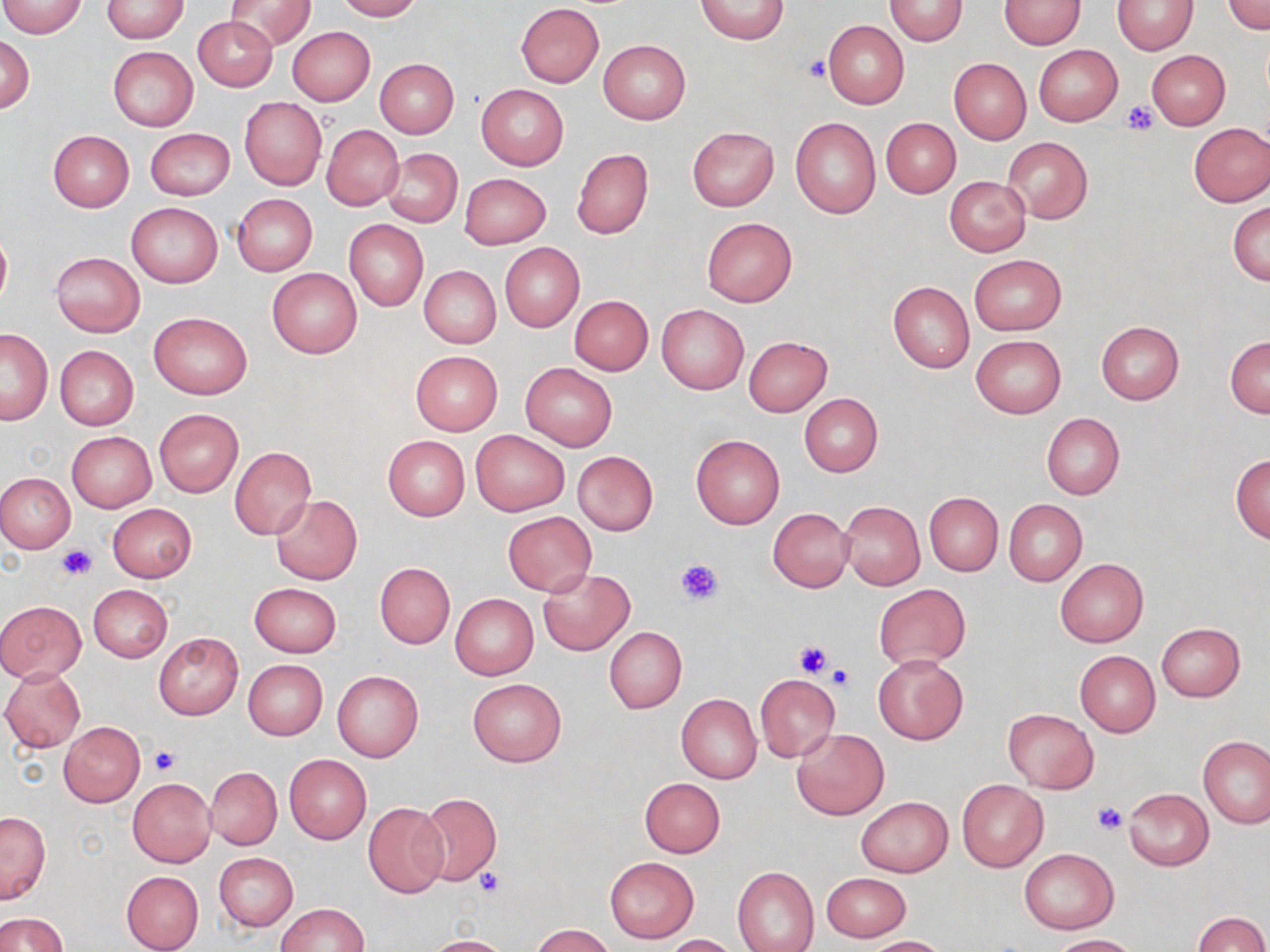
slide-level diagnosis = negative for blood parasites
preparation = thin blood smear
stain = May-Grünwald-Giemsa
image size = 1270×952 pixels
magnification = 1000x
uninfected red blood cell locations = approximate bounding boxes as [x1, y1, x2, y2] in pixels: [226, 0, 315, 51], [333, 0, 421, 21], [694, 0, 791, 45], [883, 0, 968, 45], [1224, 0, 1270, 34], [0, 1, 89, 37], [102, 1, 190, 42], [998, 1, 1086, 49], [1112, 1, 1197, 55], [516, 4, 605, 87], [193, 17, 279, 90], [822, 20, 909, 109], [288, 26, 375, 105], [1, 35, 34, 112], [598, 40, 691, 125], [1033, 44, 1123, 126], [107, 46, 199, 131], [1146, 50, 1230, 130], [949, 57, 1031, 144], [374, 58, 458, 139], [476, 84, 569, 169], [240, 98, 326, 190], [789, 116, 881, 219], [880, 117, 960, 198], [1188, 122, 1270, 206], [321, 124, 404, 210], [687, 126, 779, 211], [146, 127, 234, 200], [48, 130, 133, 212], [1001, 137, 1092, 224], [382, 148, 462, 227], [571, 148, 653, 239], [460, 173, 551, 249], [945, 176, 1032, 257], [232, 194, 317, 276], [1228, 201, 1270, 286], [127, 202, 223, 288], [702, 217, 796, 307], [344, 219, 428, 311], [0, 228, 11, 311], [499, 243, 585, 333], [51, 251, 145, 337], [969, 254, 1066, 335], [419, 266, 501, 349], [267, 268, 362, 358], [888, 281, 974, 373], [569, 295, 653, 376], [657, 305, 749, 393], [148, 311, 252, 398], [1097, 321, 1183, 404], [0, 328, 53, 425], [971, 335, 1066, 418], [742, 336, 833, 416], [1226, 336, 1270, 417], [55, 345, 139, 431], [410, 351, 503, 435], [520, 363, 617, 452], [799, 394, 883, 477], [153, 407, 244, 497], [1041, 412, 1124, 499], [67, 431, 156, 512], [470, 431, 568, 515], [690, 434, 785, 529], [382, 435, 470, 520], [230, 446, 316, 539], [573, 451, 659, 535], [1230, 453, 1270, 543], [0, 472, 75, 553], [924, 493, 1001, 576], [271, 495, 362, 583], [839, 500, 925, 589], [1004, 500, 1087, 585], [106, 503, 197, 583], [767, 507, 855, 593], [503, 512, 596, 596], [1054, 559, 1148, 648], [375, 562, 454, 648], [537, 569, 634, 656], [249, 582, 343, 658], [88, 584, 173, 662], [873, 584, 970, 669], [449, 594, 539, 679], [0, 600, 87, 682], [1155, 622, 1246, 701], [604, 626, 687, 713], [153, 631, 243, 720], [1075, 651, 1159, 737], [874, 655, 967, 744], [243, 659, 327, 740], [0, 668, 87, 753], [332, 671, 422, 762], [754, 674, 839, 762], [466, 678, 566, 767], [676, 692, 762, 784], [1003, 709, 1098, 793], [59, 722, 144, 805], [792, 727, 889, 819], [1199, 736, 1269, 829], [284, 755, 371, 843], [206, 767, 282, 851], [127, 778, 215, 867], [639, 778, 725, 858], [957, 779, 1048, 871], [1123, 788, 1214, 869], [417, 793, 502, 886], [856, 797, 952, 877], [363, 803, 449, 898], [1, 811, 51, 905], [1018, 849, 1118, 934], [215, 852, 297, 931], [605, 856, 699, 944], [732, 867, 819, 952], [121, 870, 203, 951], [821, 873, 910, 942], [277, 903, 369, 951], [1194, 911, 1269, 951], [0, 913, 67, 952], [530, 924, 616, 952], [663, 934, 742, 952], [1048, 934, 1139, 951], [423, 935, 513, 952], [863, 936, 952, 952]
modality = light microscopy
platelet locations = approximate bounding boxes as [x1, y1, x2, y2] in pixels: [803, 56, 830, 81], [1120, 101, 1159, 136], [55, 545, 96, 581], [674, 556, 725, 606], [793, 639, 836, 678], [824, 665, 855, 694], [149, 747, 178, 774], [1092, 802, 1127, 835], [474, 869, 506, 899]
field of view = one of a larger specimen